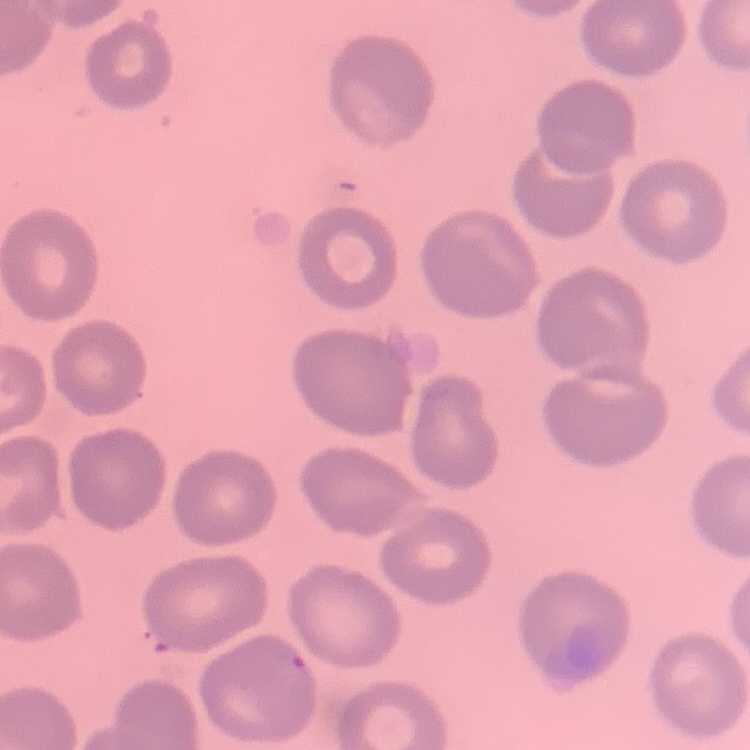

erythrocyte morphology = no rouleaux formation
preparation = thin blood smear
image type = square crop of a larger photomicrograph
stain = Field's or Giemsa